Locate every blood parasite and identify its species.
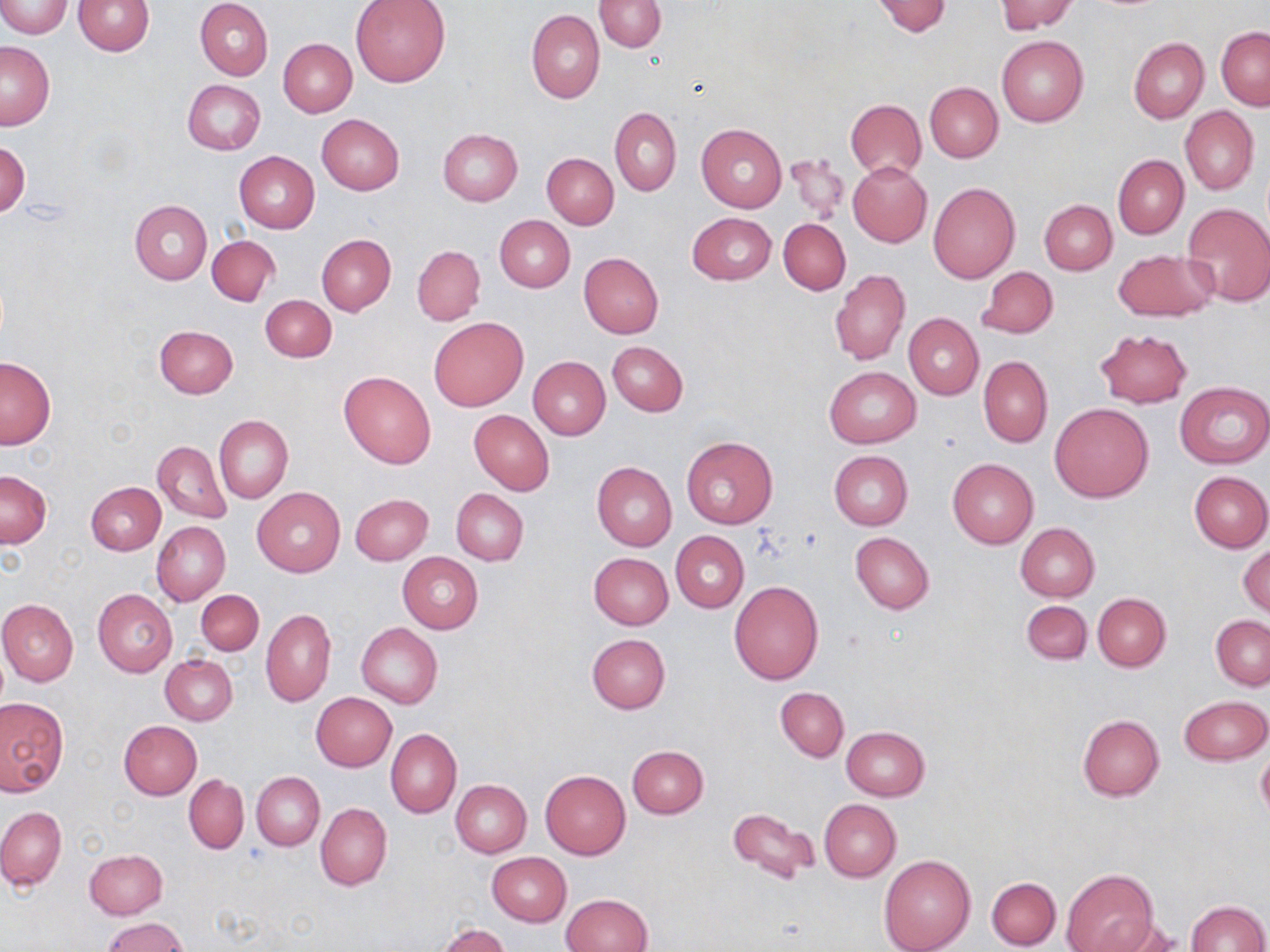
No blood parasites seen.

slide_level_diagnosis: no evidence of blood parasites
uninfected_red_blood_cell_locations: 'approximate bounding boxes as named x1/y1/x2/y2 corners in pixels: (x1=2, y1=0, x2=70, y2=38), (x1=74, y1=0, x2=155, y2=55), (x1=594, y1=0, x2=667, y2=52), (x1=995, y1=0, x2=1077, y2=34), (x1=196, y1=1, x2=272, y2=80), (x1=350, y1=1, x2=450, y2=87), (x1=871, y1=1, x2=952, y2=36), (x1=526, y1=9, x2=605, y2=104), (x1=1217, y1=26, x2=1269, y2=110), (x1=997, y1=35, x2=1088, y2=127), (x1=1129, y1=37, x2=1209, y2=124), (x1=279, y1=38, x2=357, y2=116), (x1=1, y1=42, x2=55, y2=130), (x1=183, y1=79, x2=266, y2=154), (x1=925, y1=82, x2=1002, y2=162), (x1=847, y1=99, x2=926, y2=179), (x1=1180, y1=105, x2=1258, y2=194), (x1=610, y1=107, x2=681, y2=195), (x1=316, y1=114, x2=404, y2=194), (x1=696, y1=124, x2=787, y2=212), (x1=437, y1=128, x2=523, y2=206), (x1=1, y1=139, x2=29, y2=217), (x1=784, y1=151, x2=850, y2=224), (x1=234, y1=152, x2=319, y2=234), (x1=542, y1=153, x2=618, y2=228), (x1=1113, y1=154, x2=1188, y2=239), (x1=848, y1=161, x2=932, y2=246), (x1=928, y1=182, x2=1020, y2=284), (x1=1040, y1=199, x2=1117, y2=275), (x1=129, y1=201, x2=211, y2=284), (x1=1182, y1=203, x2=1270, y2=306), (x1=687, y1=213, x2=777, y2=286), (x1=495, y1=215, x2=574, y2=292), (x1=779, y1=218, x2=850, y2=295), (x1=317, y1=234, x2=395, y2=315), (x1=207, y1=235, x2=281, y2=307), (x1=413, y1=246, x2=485, y2=324), (x1=1112, y1=248, x2=1218, y2=323), (x1=578, y1=252, x2=664, y2=338), (x1=977, y1=266, x2=1057, y2=339), (x1=829, y1=269, x2=909, y2=365), (x1=260, y1=295, x2=336, y2=363), (x1=903, y1=312, x2=984, y2=400), (x1=428, y1=317, x2=528, y2=411), (x1=154, y1=324, x2=238, y2=398), (x1=1094, y1=329, x2=1192, y2=408), (x1=607, y1=341, x2=687, y2=415), (x1=979, y1=355, x2=1052, y2=447), (x1=1, y1=357, x2=56, y2=449), (x1=529, y1=357, x2=609, y2=439), (x1=825, y1=366, x2=920, y2=449), (x1=338, y1=369, x2=437, y2=468), (x1=1175, y1=380, x2=1269, y2=469), (x1=1050, y1=402, x2=1153, y2=502), (x1=469, y1=409, x2=555, y2=495), (x1=214, y1=415, x2=292, y2=502), (x1=681, y1=435, x2=778, y2=529), (x1=152, y1=440, x2=231, y2=523), (x1=829, y1=450, x2=913, y2=530), (x1=948, y1=459, x2=1037, y2=548), (x1=591, y1=461, x2=677, y2=551), (x1=0, y1=471, x2=51, y2=547), (x1=1189, y1=471, x2=1270, y2=552), (x1=86, y1=482, x2=165, y2=555), (x1=252, y1=487, x2=345, y2=577), (x1=451, y1=488, x2=528, y2=566), (x1=351, y1=493, x2=433, y2=565), (x1=152, y1=522, x2=230, y2=605), (x1=1015, y1=522, x2=1100, y2=601), (x1=671, y1=531, x2=748, y2=611), (x1=851, y1=532, x2=933, y2=615), (x1=1239, y1=543, x2=1269, y2=618), (x1=397, y1=552, x2=482, y2=633), (x1=590, y1=553, x2=672, y2=629), (x1=729, y1=581, x2=823, y2=684), (x1=93, y1=589, x2=177, y2=677), (x1=194, y1=590, x2=263, y2=656), (x1=1093, y1=593, x2=1171, y2=671), (x1=0, y1=598, x2=79, y2=685), (x1=1021, y1=600, x2=1091, y2=664), (x1=261, y1=609, x2=335, y2=707), (x1=1211, y1=615, x2=1270, y2=690), (x1=357, y1=623, x2=443, y2=707), (x1=587, y1=633, x2=671, y2=712), (x1=160, y1=655, x2=237, y2=725), (x1=776, y1=687, x2=848, y2=761), (x1=311, y1=693, x2=395, y2=772), (x1=1180, y1=695, x2=1270, y2=765), (x1=0, y1=697, x2=67, y2=795), (x1=1077, y1=714, x2=1165, y2=801), (x1=118, y1=720, x2=202, y2=799), (x1=842, y1=726, x2=930, y2=801), (x1=385, y1=729, x2=462, y2=818), (x1=628, y1=745, x2=708, y2=818), (x1=1256, y1=749, x2=1270, y2=822), (x1=541, y1=770, x2=630, y2=860), (x1=253, y1=772, x2=324, y2=850), (x1=183, y1=774, x2=249, y2=854), (x1=451, y1=780, x2=531, y2=857), (x1=819, y1=799, x2=901, y2=881), (x1=316, y1=803, x2=391, y2=890), (x1=0, y1=807, x2=66, y2=890), (x1=728, y1=807, x2=819, y2=887), (x1=84, y1=849, x2=168, y2=919), (x1=486, y1=852, x2=571, y2=927), (x1=879, y1=854, x2=975, y2=952), (x1=1062, y1=868, x2=1159, y2=952), (x1=987, y1=877, x2=1060, y2=949), (x1=562, y1=893, x2=651, y2=952), (x1=1186, y1=901, x2=1268, y2=951), (x1=103, y1=918, x2=189, y2=951), (x1=1100, y1=919, x2=1184, y2=952), (x1=435, y1=923, x2=512, y2=952)'
field_of_view: single
modality: optical microscopy
image_size: 1270×952 pixels
stain: May-Grünwald-Giemsa
magnification: 1000x
preparation: thin blood smear